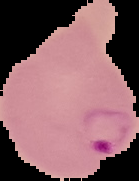
Summary:
  - Preparation: thin blood smear
  - Result: Plasmodium parasites identified
  - Image type: segmented cell region with the area outside set to black
  - Image size: 139×181 pixels